Locate every blood parasite and identify its species.
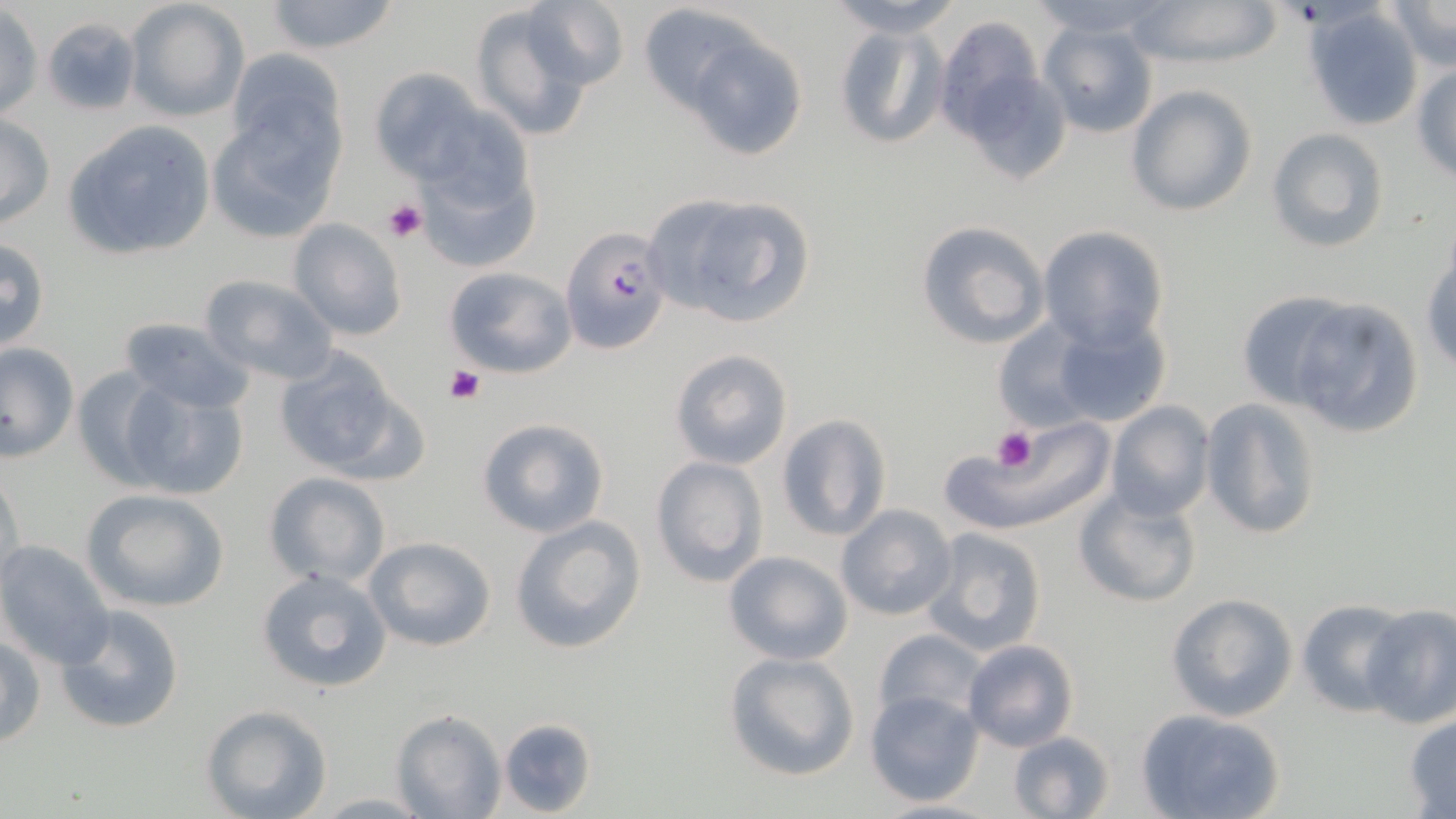

Approximate bounding boxes as named x1/y1/x2/y2 corners in pixels.
Plasmodium falciparum-infected red blood cells: (x1=560, y1=226, x2=672, y2=355).
No Plasmodium ovale, Plasmodium malariae, Plasmodium vivax, Babesia divergens, or Trypanosoma brucei observed.

Uninfected red blood cell locations: (x1=124, y1=0, x2=250, y2=123), (x1=261, y1=0, x2=406, y2=55), (x1=826, y1=0, x2=964, y2=38), (x1=1027, y1=0, x2=1168, y2=38), (x1=1130, y1=0, x2=1285, y2=68), (x1=519, y1=1, x2=631, y2=91), (x1=1384, y1=1, x2=1456, y2=73), (x1=469, y1=4, x2=601, y2=141), (x1=636, y1=4, x2=764, y2=114), (x1=0, y1=6, x2=44, y2=122), (x1=1303, y1=6, x2=1426, y2=129), (x1=933, y1=15, x2=1048, y2=141), (x1=834, y1=22, x2=945, y2=149), (x1=1037, y1=22, x2=1159, y2=140), (x1=681, y1=30, x2=809, y2=161), (x1=224, y1=48, x2=349, y2=167), (x1=951, y1=58, x2=1070, y2=184), (x1=1412, y1=65, x2=1456, y2=183), (x1=368, y1=68, x2=494, y2=186), (x1=1126, y1=86, x2=1258, y2=216), (x1=209, y1=101, x2=343, y2=242), (x1=410, y1=103, x2=548, y2=263), (x1=1, y1=113, x2=55, y2=230), (x1=61, y1=119, x2=217, y2=262), (x1=1266, y1=126, x2=1390, y2=253), (x1=643, y1=191, x2=817, y2=330), (x1=287, y1=218, x2=408, y2=342), (x1=914, y1=220, x2=1050, y2=350), (x1=1036, y1=225, x2=1171, y2=350), (x1=0, y1=236, x2=52, y2=354), (x1=1422, y1=249, x2=1456, y2=375), (x1=444, y1=266, x2=576, y2=378), (x1=198, y1=274, x2=339, y2=385), (x1=1237, y1=290, x2=1356, y2=409), (x1=1286, y1=298, x2=1425, y2=440), (x1=1043, y1=311, x2=1174, y2=429), (x1=118, y1=316, x2=253, y2=413), (x1=991, y1=319, x2=1098, y2=431), (x1=0, y1=341, x2=80, y2=462), (x1=269, y1=345, x2=421, y2=480), (x1=668, y1=348, x2=794, y2=469), (x1=70, y1=364, x2=173, y2=488), (x1=109, y1=373, x2=251, y2=500), (x1=1201, y1=398, x2=1325, y2=539), (x1=1104, y1=401, x2=1214, y2=520), (x1=775, y1=414, x2=892, y2=541), (x1=475, y1=416, x2=611, y2=538), (x1=969, y1=421, x2=1120, y2=535), (x1=650, y1=456, x2=768, y2=586), (x1=1, y1=466, x2=25, y2=591), (x1=263, y1=471, x2=393, y2=589), (x1=80, y1=487, x2=231, y2=613), (x1=1073, y1=487, x2=1203, y2=608), (x1=836, y1=504, x2=957, y2=621), (x1=508, y1=514, x2=648, y2=655), (x1=919, y1=528, x2=1048, y2=655), (x1=362, y1=536, x2=498, y2=654), (x1=0, y1=541, x2=115, y2=669), (x1=722, y1=550, x2=853, y2=666), (x1=256, y1=567, x2=393, y2=692), (x1=1164, y1=593, x2=1299, y2=722), (x1=1296, y1=598, x2=1418, y2=715), (x1=54, y1=604, x2=186, y2=734), (x1=1357, y1=604, x2=1456, y2=729), (x1=873, y1=628, x2=986, y2=725), (x1=1, y1=632, x2=46, y2=748), (x1=962, y1=639, x2=1079, y2=752), (x1=723, y1=651, x2=860, y2=781), (x1=864, y1=690, x2=984, y2=807), (x1=201, y1=705, x2=332, y2=819), (x1=392, y1=708, x2=505, y2=818), (x1=1137, y1=708, x2=1287, y2=819), (x1=1403, y1=712, x2=1456, y2=816), (x1=497, y1=718, x2=597, y2=818), (x1=1008, y1=731, x2=1117, y2=818), (x1=312, y1=792, x2=435, y2=816). Platelet locations: (x1=382, y1=199, x2=426, y2=244), (x1=447, y1=366, x2=485, y2=404), (x1=990, y1=428, x2=1038, y2=471). Slide-level diagnosis: Plasmodium falciparum. Light microscopy. May-Grünwald-Giemsa stain. Thin blood smear. Captured at 1000x magnification. Image is 1456×819 pixels. One field of a larger specimen.